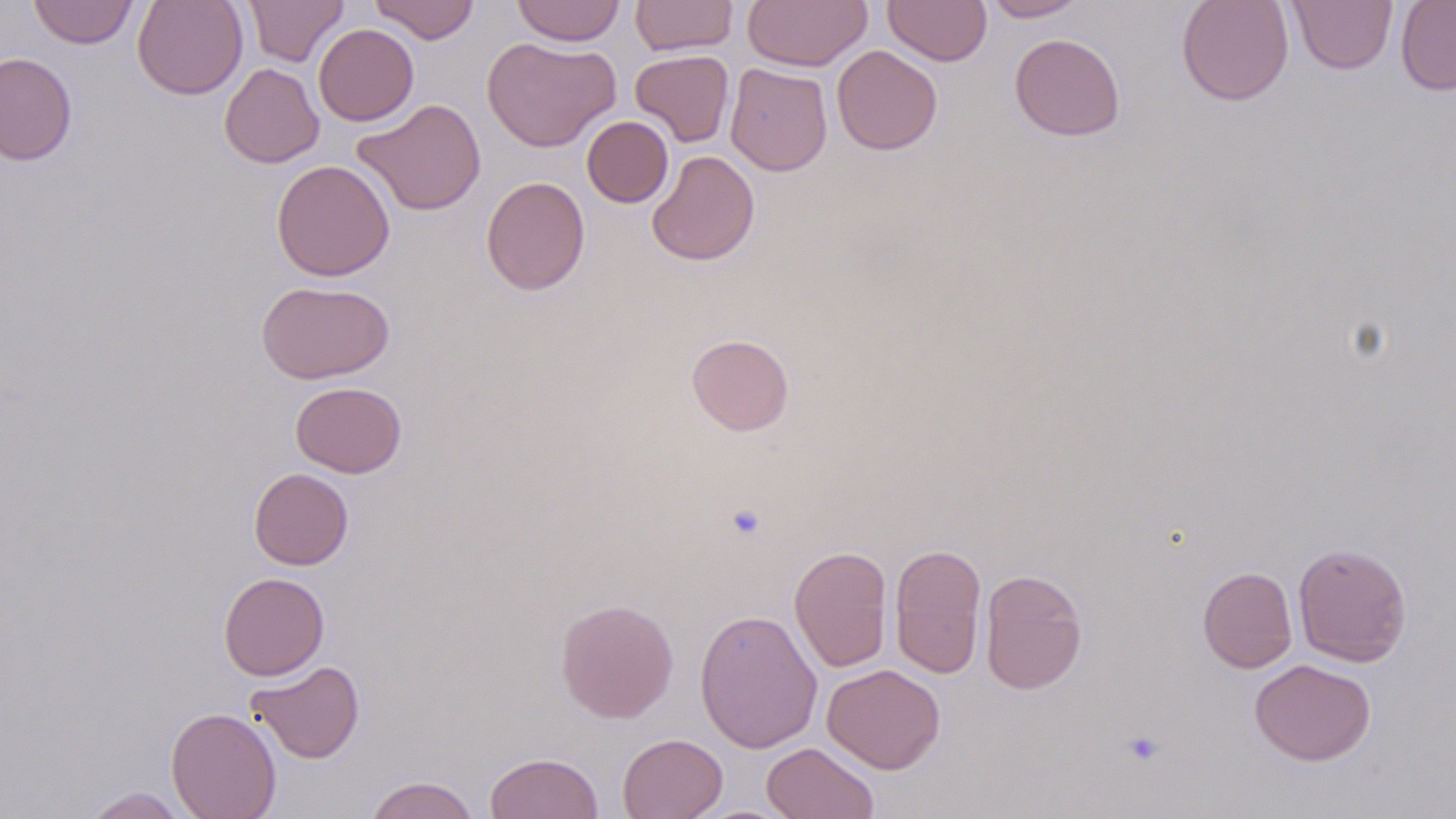

Approximate bounding boxes as (x1, y1, x2, y2) in pixels. Platelet locations: (725, 503, 767, 542), (1122, 731, 1165, 766). Uninfected red blood cell locations: (28, 0, 139, 49), (132, 0, 248, 100), (242, 0, 349, 66), (369, 0, 480, 44), (511, 0, 626, 46), (629, 0, 739, 56), (742, 0, 873, 71), (883, 0, 992, 66), (982, 0, 1088, 22), (1176, 0, 1294, 106), (1395, 0, 1456, 95), (1288, 1, 1397, 74), (313, 23, 419, 126), (1009, 33, 1125, 141), (482, 35, 621, 152), (832, 46, 942, 155), (630, 49, 734, 147), (0, 52, 78, 166), (219, 62, 324, 168), (725, 63, 833, 176), (352, 98, 487, 216), (582, 116, 674, 207), (647, 151, 759, 266), (271, 159, 395, 281), (480, 176, 591, 295), (256, 280, 394, 384), (686, 334, 794, 436), (290, 381, 407, 478), (248, 468, 354, 570), (889, 542, 987, 680), (1293, 542, 1412, 667), (789, 545, 893, 672), (1197, 566, 1297, 673), (979, 568, 1087, 695), (218, 572, 330, 680), (555, 598, 679, 723), (694, 609, 822, 753), (1249, 658, 1376, 766), (246, 660, 365, 764), (822, 663, 945, 773), (165, 707, 282, 819), (617, 733, 728, 819), (761, 742, 880, 819), (486, 752, 603, 818), (365, 776, 479, 819), (80, 787, 194, 818). Slide-level diagnosis: negative for blood parasites. Thin blood film. Single field of view. 1000x magnification. Light microscopy. May-Grünwald-Giemsa-stained preparation. Image is 1456×819 pixels.